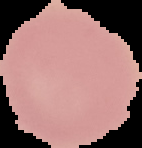

Image is 142×148 pixels. Malaria status: uninfected. From a thin blood smear. Segmented cell region on a black background.